Locate every blood parasite and identify its species.
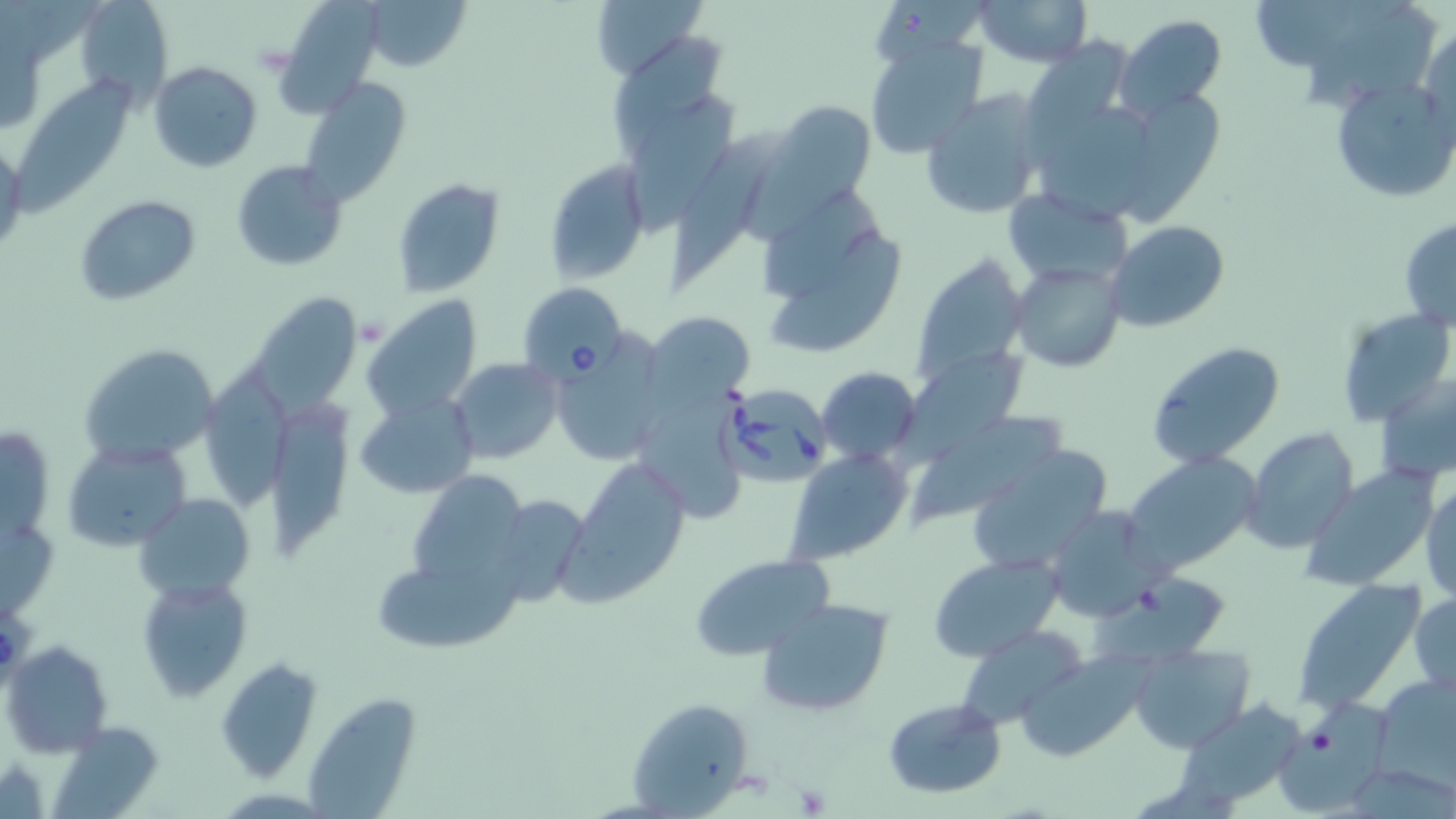
Approximate bounding boxes as [x1, y1, x2, y2] in pixels.
Babesia divergens-infected red blood cells: [517, 282, 627, 385], [721, 388, 833, 485].
No Plasmodium falciparum, Plasmodium ovale, Plasmodium malariae, Plasmodium vivax, or Trypanosoma brucei observed.

slide-level diagnosis = Babesia divergens
platelet locations = approximate bounding boxes as [x1, y1, x2, y2] in pixels: [794, 781, 833, 816]
modality = light microscopy
preparation = thin blood film
magnification = 1000x
image size = 1456×819 pixels
uninfected red blood cell locations = approximate bounding boxes as [x1, y1, x2, y2] in pixels: [279, 0, 380, 117], [362, 0, 473, 72], [587, 0, 705, 81], [971, 0, 1094, 70], [78, 1, 171, 103], [1300, 5, 1436, 111], [1115, 12, 1229, 118], [1418, 22, 1455, 142], [613, 32, 725, 157], [864, 34, 989, 159], [1018, 35, 1134, 169], [150, 61, 262, 172], [12, 78, 145, 221], [298, 78, 410, 207], [1331, 78, 1453, 205], [1122, 88, 1229, 222], [918, 90, 1047, 220], [626, 94, 736, 233], [766, 100, 878, 209], [1040, 107, 1164, 224], [665, 127, 791, 291], [0, 140, 26, 261], [542, 159, 651, 283], [231, 160, 348, 270], [392, 177, 507, 298], [1002, 187, 1134, 287], [73, 194, 200, 307], [760, 194, 881, 306], [1398, 218, 1456, 332], [1107, 221, 1229, 333], [774, 235, 908, 351], [912, 253, 1028, 389], [1010, 259, 1125, 371], [247, 286, 355, 420], [363, 295, 484, 420], [1335, 306, 1454, 427], [644, 309, 758, 408], [1145, 340, 1287, 469], [78, 343, 221, 466], [551, 344, 666, 466], [895, 345, 1033, 470], [449, 358, 562, 464], [816, 366, 921, 464], [205, 367, 299, 510], [1377, 373, 1456, 487], [356, 392, 480, 498], [642, 393, 746, 518], [916, 408, 1066, 528], [272, 413, 350, 558], [1242, 429, 1359, 554], [61, 439, 188, 555], [971, 445, 1113, 575], [786, 448, 912, 562], [1123, 453, 1260, 575], [565, 456, 694, 605], [1299, 467, 1444, 594], [412, 472, 527, 594], [1422, 482, 1456, 600], [485, 491, 594, 606], [136, 492, 255, 600], [1042, 506, 1163, 625], [688, 553, 837, 661], [929, 553, 1063, 662], [375, 563, 524, 652], [1094, 572, 1240, 678], [137, 575, 253, 703], [1291, 585, 1429, 710], [1410, 591, 1456, 699], [758, 600, 893, 716], [956, 625, 1090, 730], [4, 641, 112, 756], [1130, 643, 1254, 753], [1016, 654, 1144, 761], [216, 658, 321, 780], [1372, 672, 1455, 789], [307, 692, 420, 819], [625, 697, 757, 812], [882, 697, 1006, 800], [1176, 700, 1309, 807], [1272, 701, 1393, 814], [48, 722, 162, 816]
field of view = single
stain = May-Grünwald-Giemsa